Locate Plasmodium parasites and leukocytes.
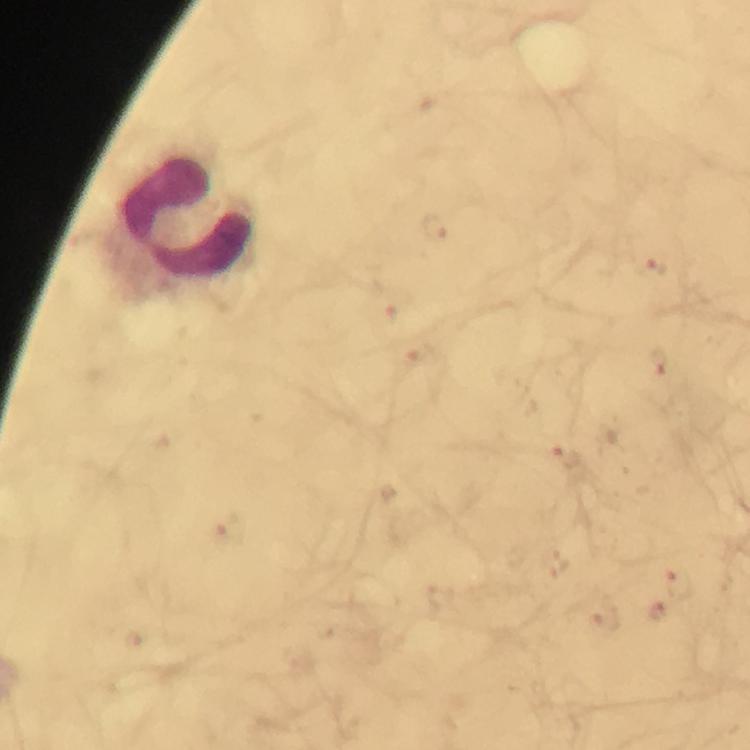
Approximate object centers, in pixels from the top-left corner.
Plasmodium parasites: (x=439, y=228), (x=657, y=266), (x=659, y=364), (x=567, y=457), (x=677, y=586), (x=656, y=612), (x=606, y=618).
Leukocytes: (x=188, y=215).

Photographed with a smartphone mounted on the microscope. Giemsa-stained preparation. 100x magnification. Immersion oil applied. From a malaria diagnostic workup. Cropped region of a single field of view. Image is 750×750 pixels. Thick blood film.